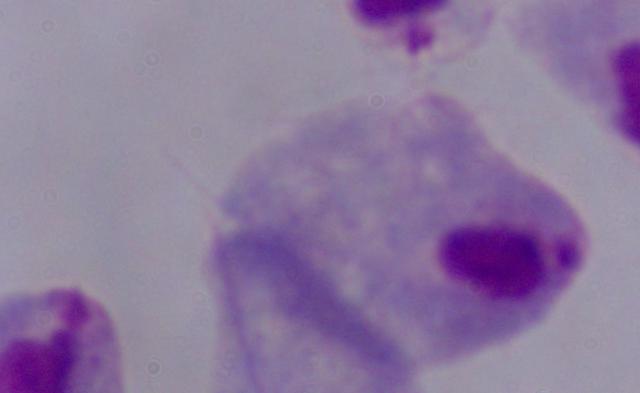
Summary:
  - Magnification: 1000x
  - Modality: photomicrograph
  - Identification: trichomonad